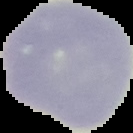

malaria status = uninfected
preparation = thin blood smear
image type = segmented cell region on a black background
image size = 133×133 pixels